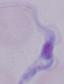

Summary:
  - Modality: micrograph
  - Magnification: 1000x
  - Identification: trypanosome